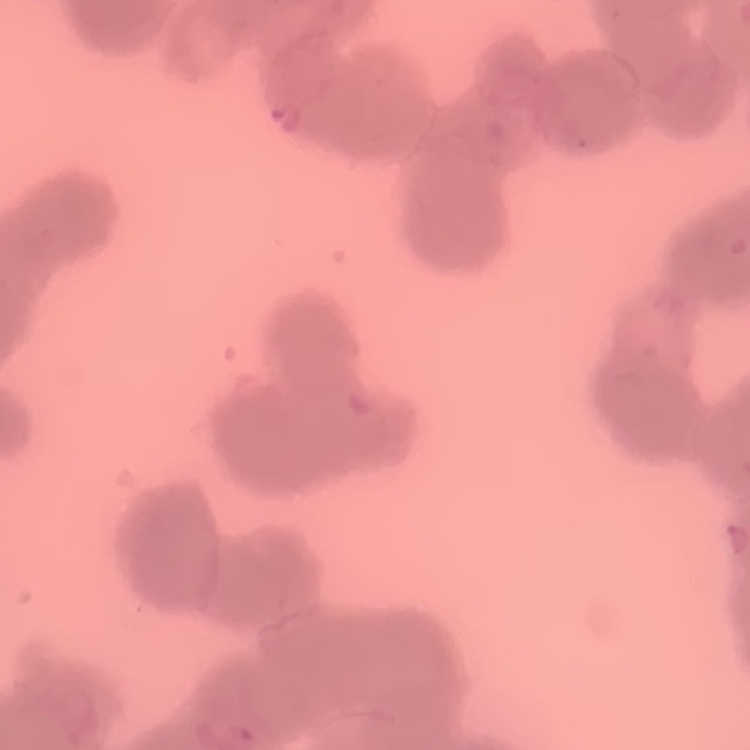 The red blood cells show rouleaux formation. Field's or Giemsa stain. Thin peripheral smear. One tile cut from a larger photomicrograph.